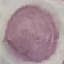

Result: negative for malaria parasites. Cell patch, automatically extracted from a larger field of view and resized to 64 × 64 pixels. Thin blood smear. Acquired by smartphone through the microscope eyepiece. Giemsa stain.